Classify this cell by malaria status.
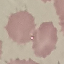

It is uninfected.

Summary:
  - Stain: Giemsa
  - Image type: automatically extracted cell patch, resized to 64 × 64 pixels
  - Preparation: thin smear
  - Capture: smartphone through the microscope eyepiece